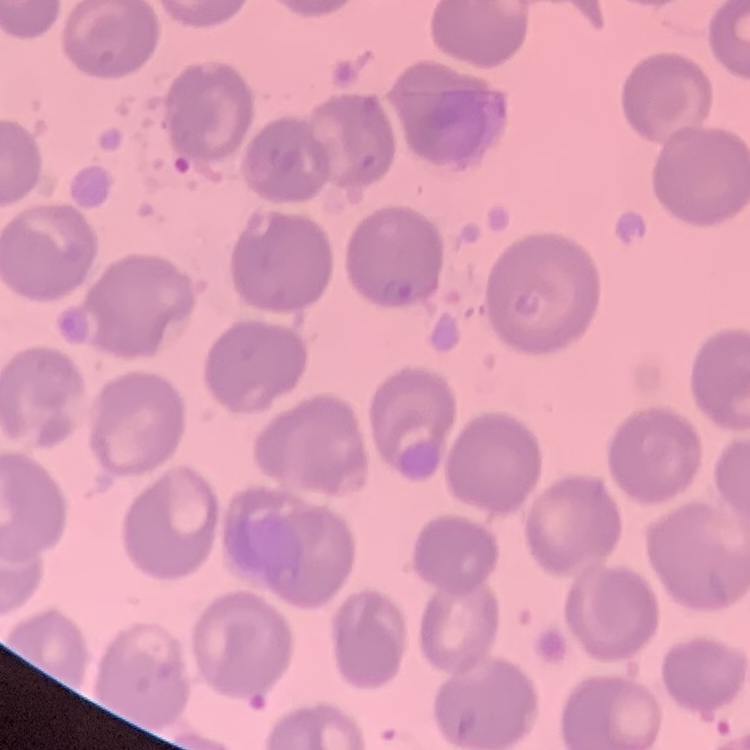
The erythrocytes exhibit no rouleaux formation. Thin peripheral smear. Square crop of a larger photomicrograph. Stained with either Field's or Giemsa.